Point out every malaria parasite.
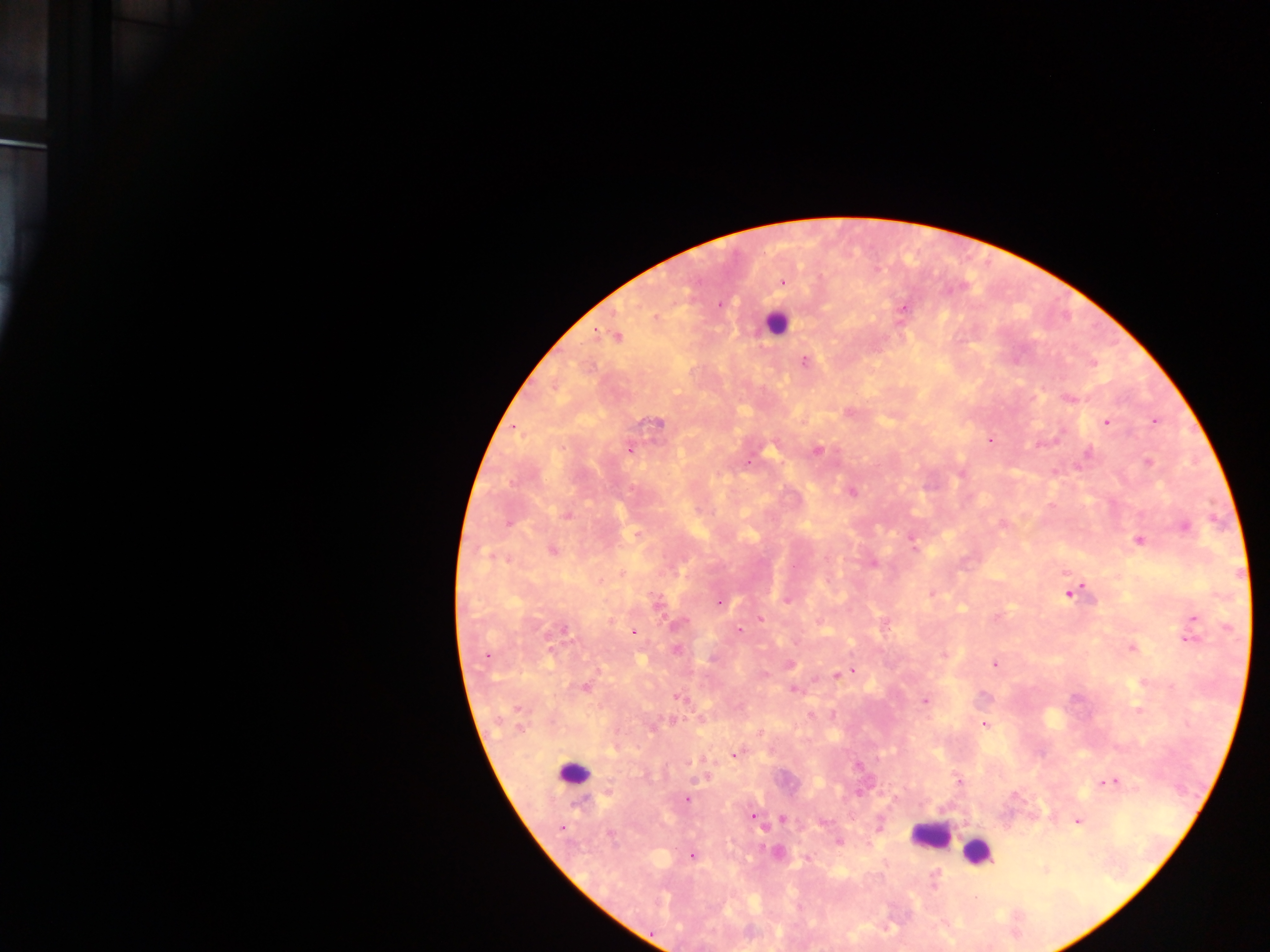
Approximate centers as [x, y] in pixels.
Malaria parasites: [782, 281], [718, 305], [904, 308], [654, 316], [616, 336], [805, 360], [1091, 362], [1068, 398], [850, 412], [1154, 421], [1106, 422], [655, 423], [513, 426], [988, 439], [1038, 444], [630, 448], [816, 449], [1087, 453], [748, 462], [1148, 463], [852, 491], [566, 515], [1002, 524], [1184, 526], [636, 534], [910, 537], [1138, 541], [551, 549], [873, 563], [621, 573], [599, 581], [1071, 590], [787, 598], [719, 601], [656, 603], [995, 617], [760, 618], [1193, 618], [677, 625], [739, 630], [633, 632], [1189, 636], [1131, 647], [676, 649], [487, 655], [788, 663], [994, 663], [852, 671], [836, 676], [584, 687], [793, 689], [678, 696], [925, 700], [1138, 710], [984, 723], [734, 755], [859, 766], [959, 781], [1111, 782], [687, 798], [752, 816], [782, 819], [1077, 820], [560, 829], [838, 841], [776, 853], [691, 855], [1044, 870].

image size = 1270×952 pixels
country = Ghana
preparation = thick blood film
capture = mobile-phone photograph through a microscope
field of view = single
leukocyte locations = approximate centers as [x, y] in pixels: [775, 322], [573, 774], [931, 836], [977, 851]